Give the position of every Plasmodium parasite visible.
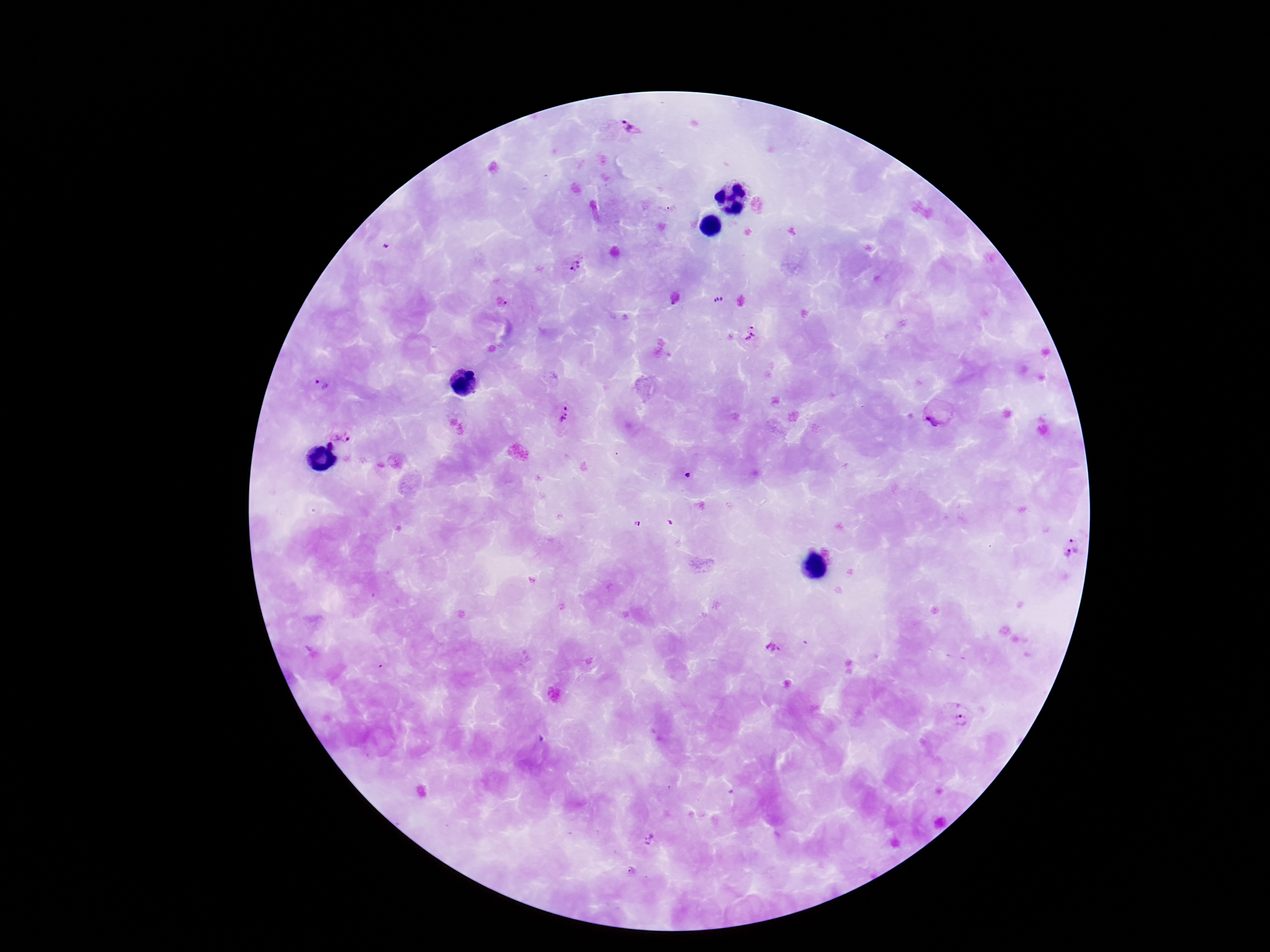

Approximate centers as {x, y} in pixels.
Plasmodium parasites: {631, 128}, {671, 208}, {574, 267}, {502, 301}, {752, 336}, {323, 386}, {565, 416}, {936, 416}, {340, 434}, {330, 446}, {1072, 547}, {775, 648}, {962, 721}, {632, 870}.

field_of_view: one from this slide
image_size: 1270×952 pixels
patient_malaria_status: positive
capture: smartphone camera through the microscope eyepiece
magnification: 100x
stain: Giemsa
preparation: thick blood film